Assess this cell for malaria.
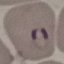

Parasitized.

Summary:
  - Preparation: thin blood film
  - Stain: Giemsa
  - Capture: smartphone through the microscope eyepiece
  - Image type: automatically extracted cell patch, resized to 64 × 64 pixels